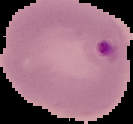
image size = 133×124 pixels
preparation = thin blood smear
image type = segmented cell region on a black background
result = Plasmodium parasites identified